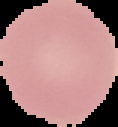 Image is 118×127 pixels. The area outside the segmented cell region is set to black. From a thin blood smear. Malaria status: uninfected.